Outline each blood parasite and name the species.
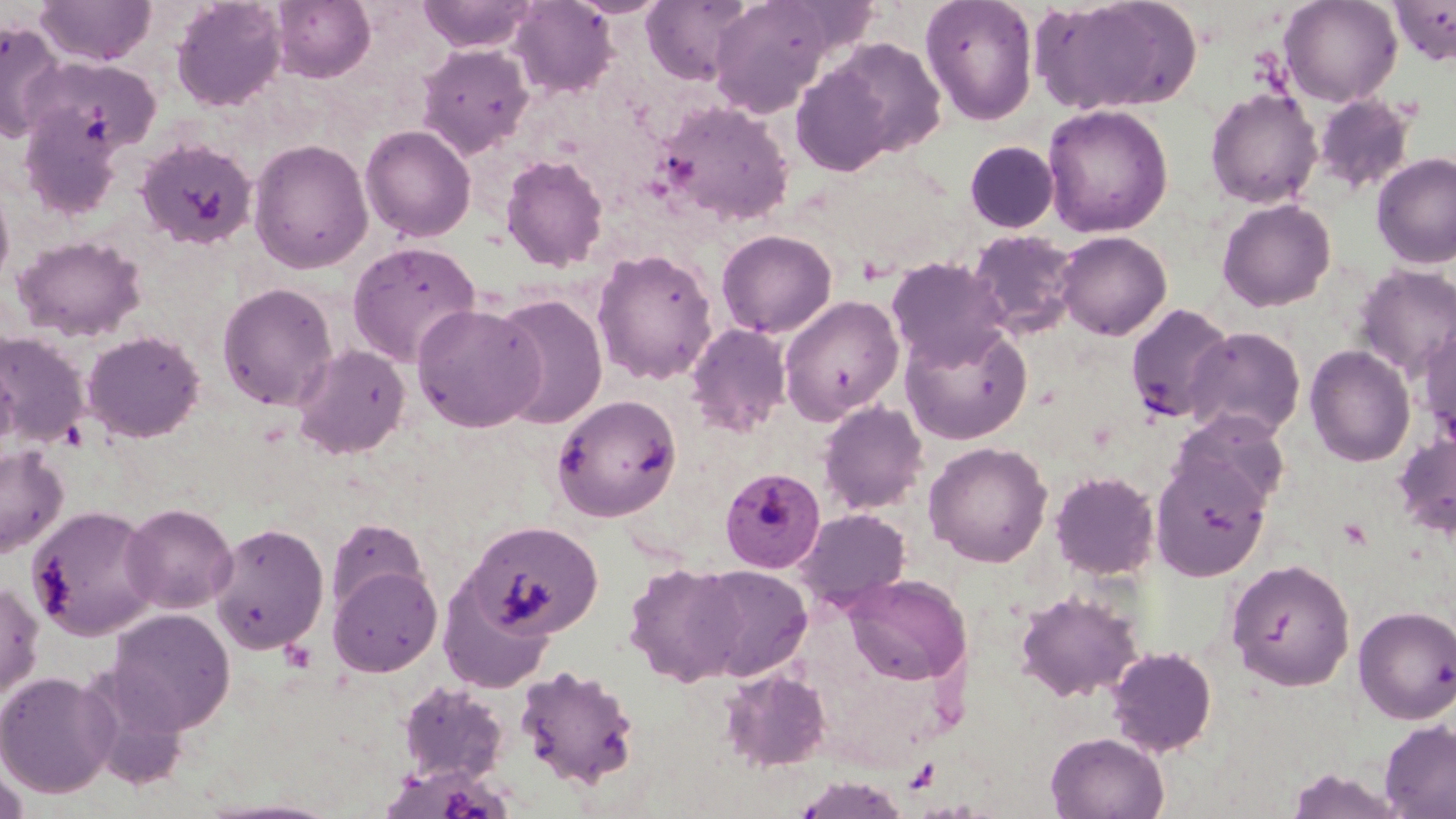

Approximate bounding boxes as (x1,y1)-(x2,y2) corner pairs in pixels.
Plasmodium malariae-infected red blood cells: (719,467)-(826,573).
No Plasmodium falciparum, Plasmodium ovale, Plasmodium vivax, Babesia divergens, or Trypanosoma brucei observed.

Uninfected red blood cell locations: (35,0)-(157,67), (170,0)-(287,112), (270,0)-(376,83), (417,0)-(539,52), (640,0)-(753,84), (706,0)-(843,118), (919,0)-(1039,126), (1035,0)-(1202,116), (1278,0)-(1403,107), (1388,0)-(1456,67), (508,1)-(618,98), (0,20)-(66,141), (819,36)-(948,161), (416,43)-(534,160), (25,55)-(161,155), (789,63)-(899,176), (1204,87)-(1322,209), (1311,94)-(1417,197), (654,98)-(796,227), (18,104)-(124,221), (1042,104)-(1173,238), (360,125)-(477,243), (135,138)-(258,250), (248,138)-(374,274), (964,140)-(1059,233), (1371,152)-(1456,270), (499,153)-(609,272), (0,182)-(15,296), (1216,198)-(1336,312), (715,229)-(837,338), (967,229)-(1080,339), (1055,230)-(1172,341), (12,234)-(147,342), (346,240)-(482,367), (591,248)-(719,385), (886,257)-(1011,371), (1352,263)-(1456,381), (217,282)-(338,411), (493,293)-(608,431), (779,295)-(903,424), (411,302)-(546,433), (1125,303)-(1236,424), (899,322)-(1032,445), (685,323)-(792,437), (1418,325)-(1456,448), (1184,326)-(1306,441), (81,329)-(205,444), (0,331)-(91,448), (292,343)-(410,459), (1304,345)-(1416,467), (0,348)-(19,465), (551,393)-(683,522), (817,400)-(929,515), (1171,408)-(1291,515), (1392,431)-(1456,539), (923,441)-(1053,568), (0,444)-(69,557), (1150,452)-(1272,581), (1049,470)-(1160,580), (120,503)-(237,614), (27,505)-(161,640), (794,508)-(912,609), (326,517)-(426,620), (463,520)-(603,640), (208,521)-(329,656), (1225,558)-(1355,690), (623,562)-(745,686), (328,563)-(443,677), (687,564)-(812,681), (843,574)-(971,686), (0,581)-(44,700), (438,581)-(555,693), (1014,590)-(1142,702), (1352,605)-(1456,724), (107,608)-(235,735), (1106,645)-(1219,757), (514,663)-(642,791), (717,666)-(835,772), (0,670)-(118,799), (397,679)-(510,786), (1379,719)-(1456,818), (1045,732)-(1170,819), (1,763)-(31,819), (1283,767)-(1407,818). Slide-level diagnosis: Plasmodium malariae. Image is 1456×819 pixels. May-Grünwald-Giemsa stain. Single field of view. Captured at 1000x magnification. Thin blood smear. Optical microscopy.